Identify the parasite.
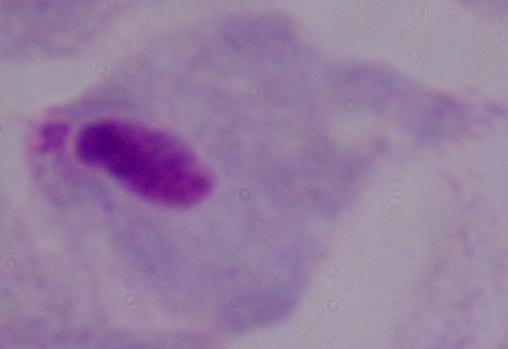

A trichomonad.

Photomicrograph. Captured at 1000x magnification.